Comment on the morphology of the red blood cells.
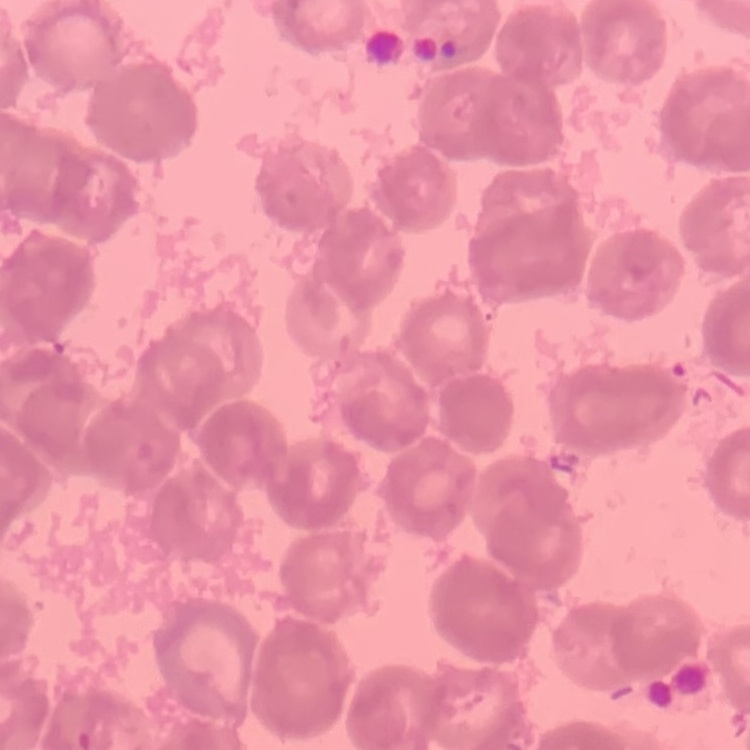

Rouleaux formation.

One tile cut from a larger photomicrograph. Thin blood film. Stained with either Field's or Giemsa.